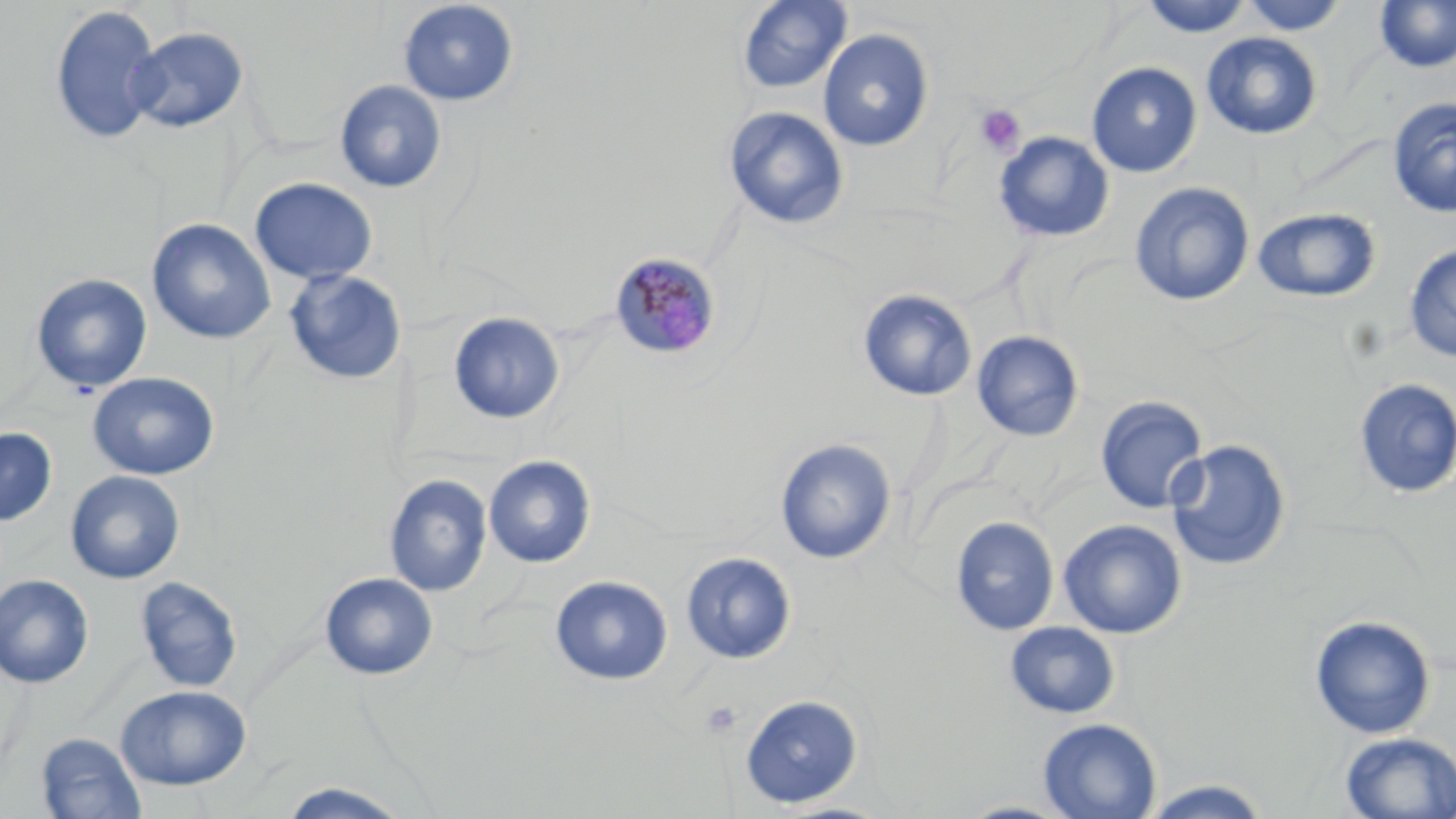

slide-level diagnosis = Plasmodium malariae
field of view = one of a larger specimen
modality = optical microscopy
magnification = 1000x
uninfected red blood cell locations = approximate bounding boxes as (x1,y1)-(x2,y2) corner pairs in pixels: (736,0)-(852,94), (1140,0)-(1255,38), (1240,0)-(1349,36), (397,1)-(520,106), (1374,1)-(1456,73), (50,4)-(163,146), (128,27)-(249,133), (818,28)-(934,152), (1201,32)-(1323,141), (1086,61)-(1202,178), (334,79)-(447,194), (1388,98)-(1456,217), (724,106)-(850,230), (993,131)-(1114,243), (249,177)-(377,285), (1129,181)-(1254,307), (1252,207)-(1381,303), (148,218)-(276,344), (1403,244)-(1456,361), (284,268)-(408,386), (30,273)-(153,392), (857,288)-(978,401), (448,311)-(565,425), (972,331)-(1084,442), (88,372)-(219,480), (1353,378)-(1456,499), (1095,396)-(1209,514), (0,427)-(57,525), (774,438)-(897,564), (1166,438)-(1291,571), (484,455)-(596,568), (65,470)-(185,584), (385,475)-(492,597), (950,516)-(1059,636), (1058,518)-(1187,639), (681,552)-(796,664), (320,572)-(438,679), (0,574)-(94,687), (135,575)-(243,692), (550,575)-(673,686), (1309,614)-(1436,739), (1004,621)-(1120,719), (117,684)-(250,790), (740,693)-(863,809), (1037,717)-(1162,819), (36,732)-(147,819), (1338,732)-(1456,818), (1138,779)-(1275,818), (275,782)-(415,819), (951,799)-(1082,818), (766,800)-(899,819)
Plasmodium malariae-infected red blood cell locations = approximate bounding boxes as (x1,y1)-(x2,y2) corner pairs in pixels: (610,252)-(722,361)
stain = May-Grünwald-Giemsa
image size = 1456×819 pixels
platelet locations = approximate bounding boxes as (x1,y1)-(x2,y2) corner pairs in pixels: (974,104)-(1027,157), (700,701)-(743,738)
preparation = thin blood smear